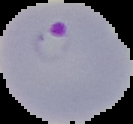
Segmented cell region on a black background. Malaria status: parasitized. From a thin blood film. Image is 133×124 pixels.